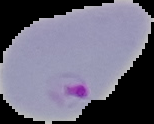

preparation: thin blood film
result: Plasmodium parasites detected
image_size: 154×124 pixels
image_type: cell region segmented out of the field of view; surrounding area masked to black